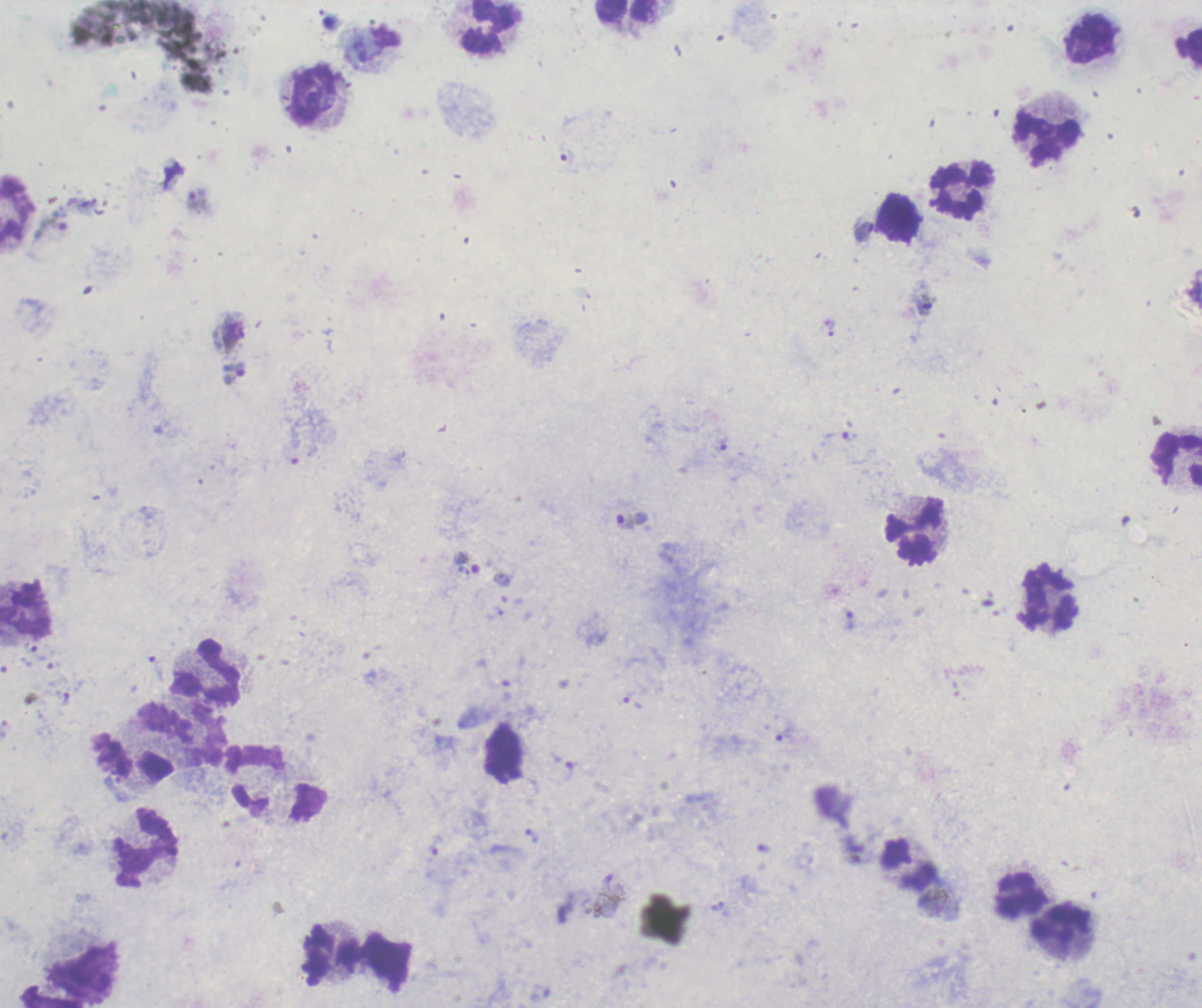

Approximate centers as (x, y) in pixels. Gametocyte locations: (923, 307). Leukocyte locations: (627, 12), (489, 27), (1090, 40), (1189, 48), (315, 96), (1047, 138), (962, 190), (16, 210), (899, 218), (1176, 458), (914, 533), (1051, 600), (25, 609), (207, 671), (256, 780), (145, 847), (910, 865), (1022, 894), (1062, 924), (332, 955), (84, 972). Trophozoite locations: (198, 201), (863, 233), (830, 328), (234, 373), (722, 445), (632, 521), (850, 620), (633, 703), (786, 735), (532, 836), (433, 851). Life-cycle stages observed: trophozoite, gametocyte. One field from this slide. Previously used in a real diagnosis. Image is 1202×1008 pixels. Result: Plasmodium parasites identified. Thick blood film. 100x magnification. Romanowsky stain. Background quality: poor.